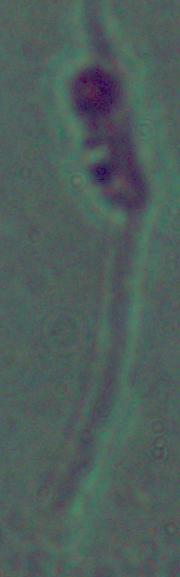

identification = Leishmania
modality = micrograph
magnification = 1000x